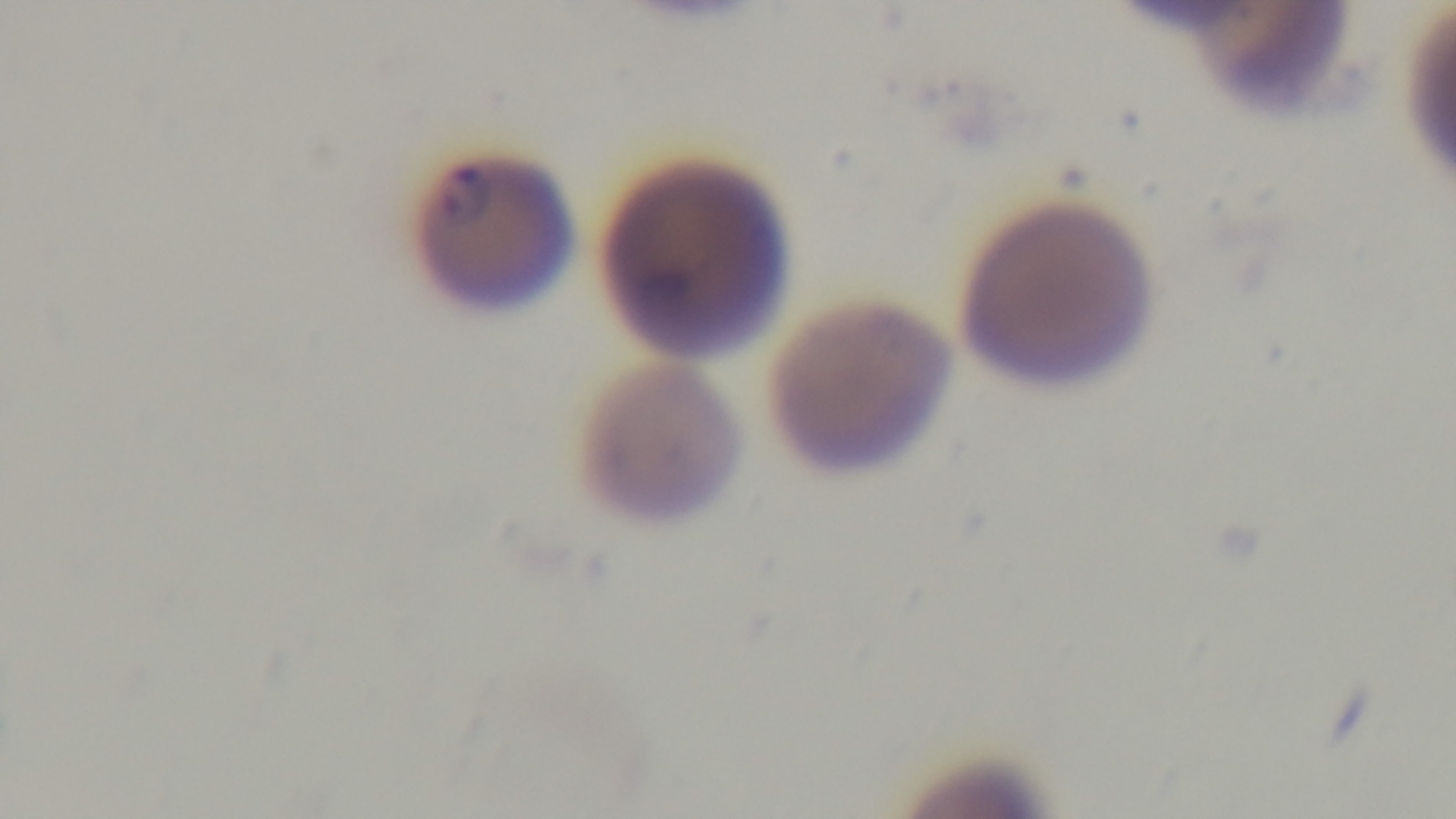

Giemsa stain. Malaria status: infected. Mounted 4K digital camera. One field from the slide. Preparation: thin smear. Light microscopy. Oil-immersion objective, 100x.